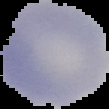
Summary:
  - Image size: 109×109 pixels
  - Malaria status: uninfected
  - Image type: segmented cell region on a black background
  - Preparation: thin blood smear